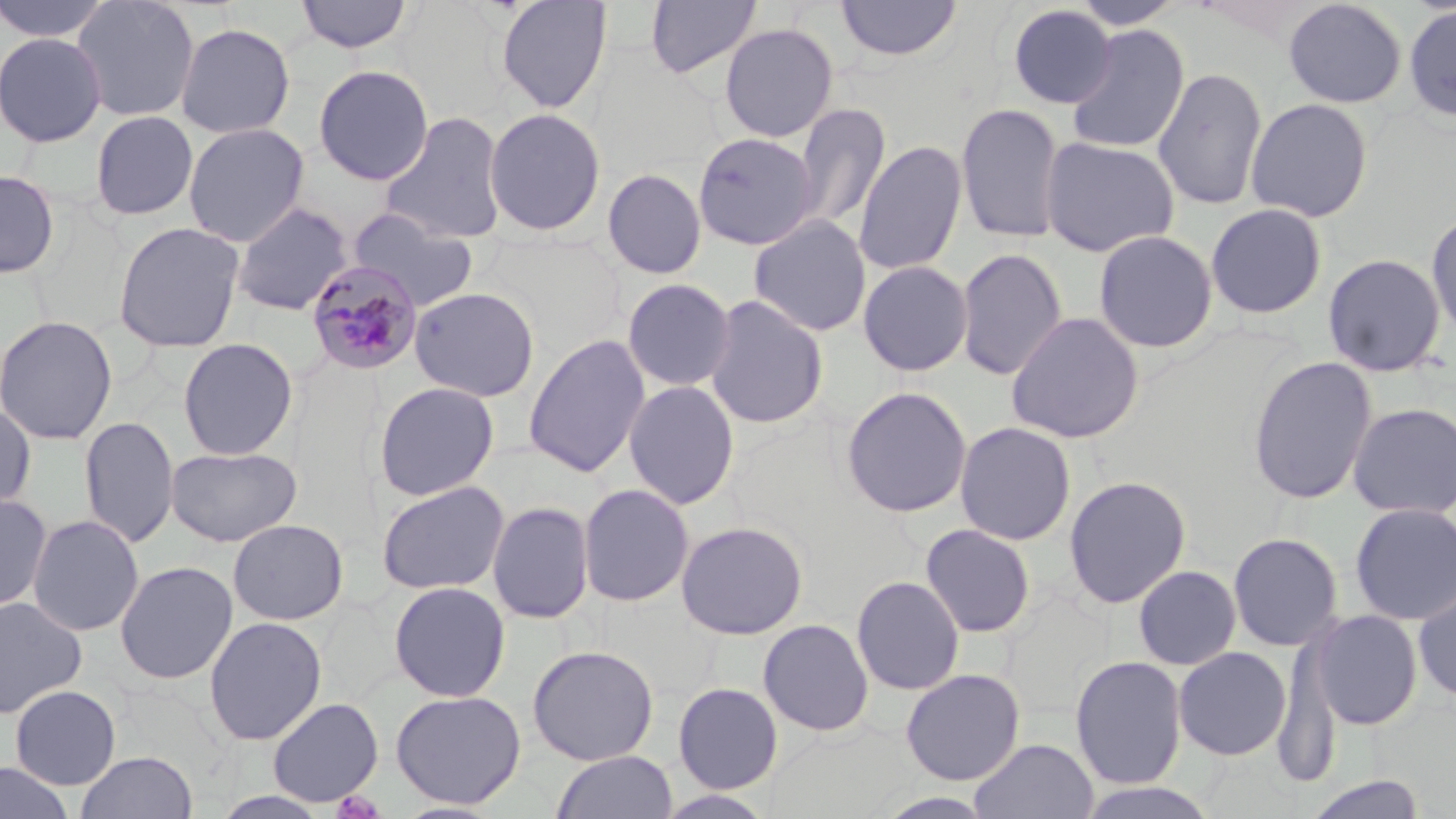
Approximate bounding boxes as (x1,y1)-(x2,y2) corner pairs in pixels. Uninfected red blood cell locations: (0,0)-(111,42), (71,0)-(201,122), (295,0)-(414,54), (495,0)-(612,114), (645,0)-(762,79), (835,0)-(962,61), (1070,0)-(1186,30), (1283,0)-(1408,109), (1007,4)-(1116,109), (1402,4)-(1456,123), (174,21)-(296,139), (719,22)-(838,142), (1065,25)-(1190,155), (0,31)-(107,148), (313,64)-(434,185), (1153,66)-(1268,210), (1245,97)-(1374,223), (792,102)-(891,232), (955,102)-(1066,244), (483,107)-(607,237), (89,110)-(199,220), (379,111)-(508,243), (183,122)-(310,247), (692,132)-(820,250), (1040,136)-(1180,257), (853,139)-(967,276), (602,168)-(707,279), (0,169)-(60,279), (231,202)-(353,316), (1206,202)-(1328,319), (347,208)-(479,312), (1426,208)-(1456,342), (748,215)-(872,337), (112,221)-(245,353), (1093,229)-(1218,353), (955,248)-(1068,381), (1322,253)-(1447,377), (857,260)-(973,377), (622,278)-(736,392), (408,286)-(540,402), (703,294)-(829,429), (1005,311)-(1145,444), (0,314)-(118,446), (523,333)-(651,477), (177,337)-(299,461), (1246,355)-(1379,505), (623,379)-(740,509), (373,381)-(500,501), (840,386)-(973,518), (1347,402)-(1456,520), (0,403)-(36,515), (78,415)-(180,549), (954,421)-(1076,545), (165,445)-(302,547), (1063,475)-(1192,608), (376,480)-(510,595), (578,483)-(695,607), (0,492)-(53,613), (487,500)-(594,624), (1349,502)-(1456,626), (27,514)-(145,637), (227,518)-(349,625), (675,520)-(808,640), (920,523)-(1036,638), (1227,532)-(1344,651), (114,561)-(238,684), (1133,564)-(1242,670), (851,575)-(964,695), (388,581)-(511,702), (1413,582)-(1456,705), (0,595)-(87,719), (1309,609)-(1423,730), (204,615)-(327,746), (758,619)-(874,736), (527,644)-(659,766), (1173,646)-(1292,761), (1070,655)-(1188,789), (900,668)-(1026,785), (672,682)-(783,793), (9,685)-(122,790), (390,689)-(526,809), (267,697)-(383,807), (969,738)-(1099,819), (75,750)-(197,819), (551,750)-(678,819), (0,762)-(75,819), (1302,775)-(1428,819), (1074,781)-(1222,819). Plasmodium malariae-infected red blood cell locations: (306,260)-(424,376). Slide-level diagnosis: Plasmodium malariae. Image is 1456×819 pixels. Captured at 1000x magnification. Light microscopy. Single field of view. May-Grünwald-Giemsa-stained preparation. Thin blood film.